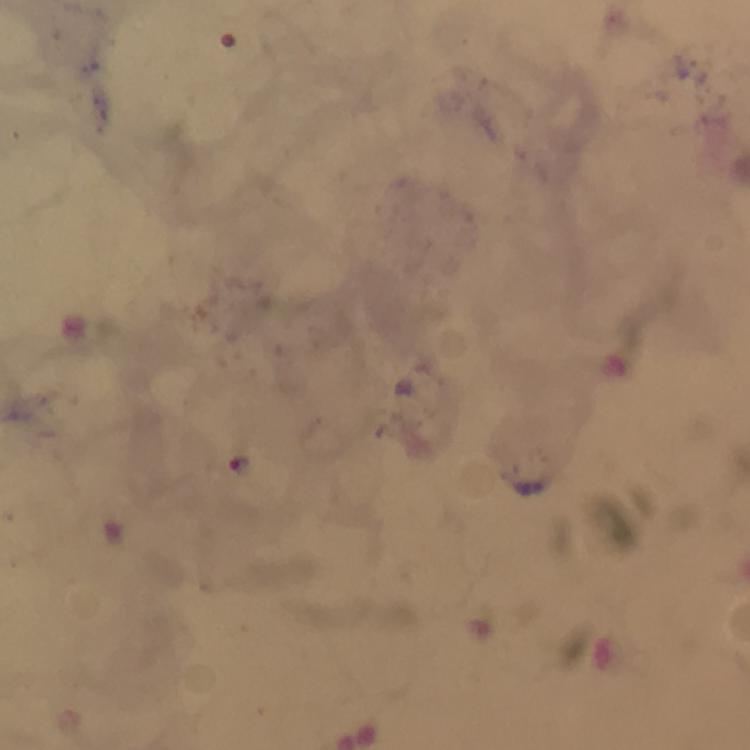

{
  "immersion_oil": "applied",
  "malaria_parasite_locations": "approximate centers as [x, y] in pixels: [240, 464]",
  "magnification": "100x",
  "capture": "smartphone mounted on the microscope",
  "cropped_from": "a single field of view",
  "image_size": "750×750 pixels",
  "stain": "Giemsa",
  "preparation": "thick blood film",
  "context": "from a diagnostic examination for malaria"
}